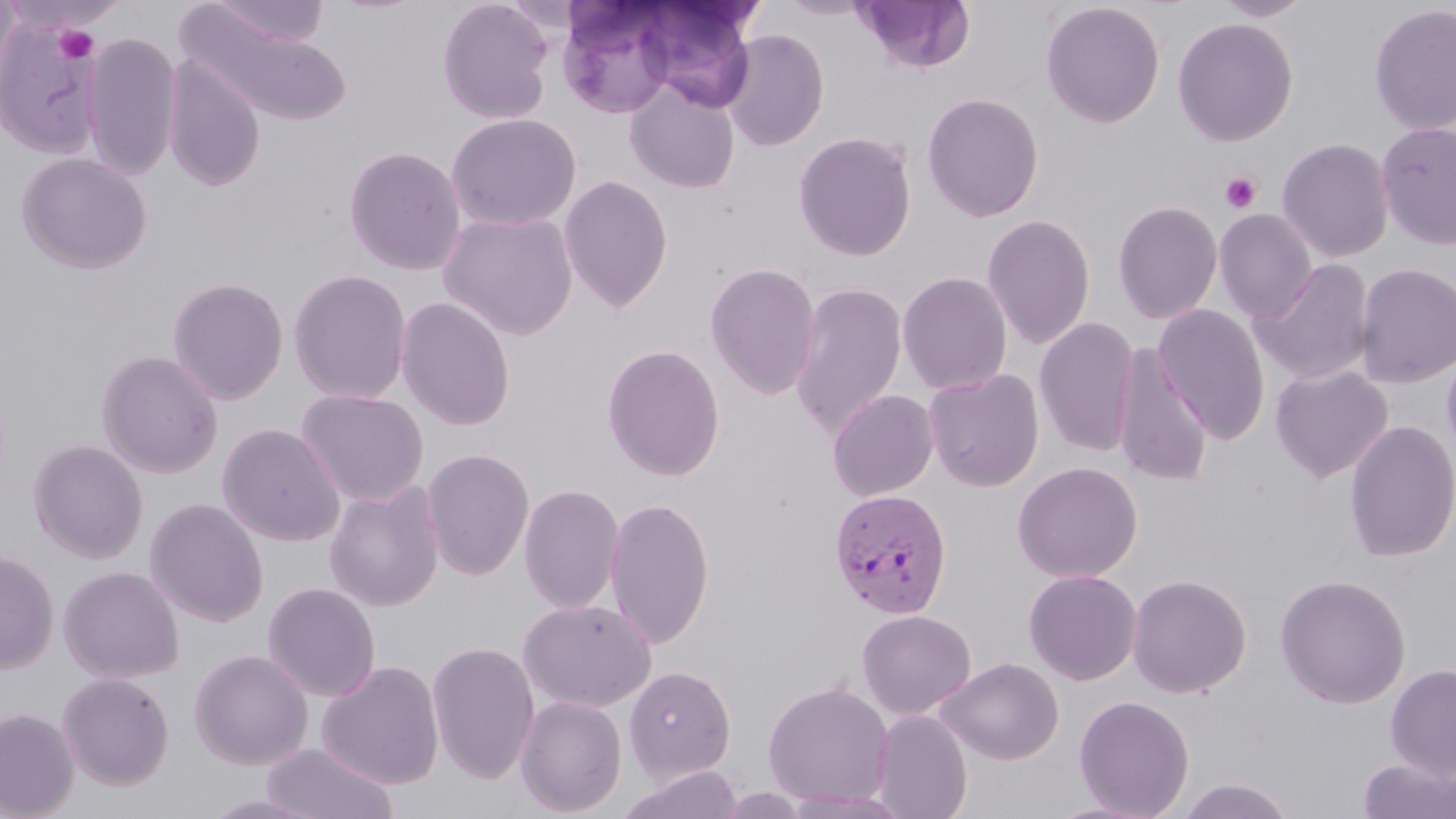

Summary:
  - Coordinate format: approximate bounding boxes as [x1, y1, x2, y2] in pixels
  - Platelet locations: [54, 24, 97, 62], [1220, 171, 1262, 214]
  - Plasmodium vivax-infected red blood cell locations: [828, 488, 953, 618]
  - Uninfected red blood cell locations: [0, 0, 23, 104], [208, 0, 331, 47], [437, 0, 555, 124], [776, 0, 877, 19], [854, 0, 977, 74], [1212, 0, 1317, 22], [633, 1, 759, 110], [1041, 1, 1165, 128], [558, 2, 678, 117], [1368, 3, 1456, 136], [179, 6, 351, 126], [0, 11, 105, 161], [1173, 17, 1298, 147], [720, 29, 829, 151], [83, 32, 182, 181], [162, 56, 266, 192], [625, 79, 741, 194], [922, 92, 1044, 223], [446, 113, 581, 231], [1376, 121, 1456, 251], [793, 131, 917, 262], [1277, 138, 1394, 263], [344, 145, 467, 276], [16, 152, 153, 275], [558, 174, 674, 313], [1112, 200, 1223, 325], [1214, 209, 1317, 322], [439, 210, 579, 340], [981, 213, 1096, 349], [1251, 259, 1376, 385], [704, 262, 822, 401], [1354, 262, 1456, 389], [289, 269, 412, 404], [897, 271, 1013, 395], [167, 277, 289, 404], [789, 281, 908, 440], [395, 297, 516, 431], [1153, 305, 1271, 444], [1034, 318, 1140, 457], [602, 343, 726, 482], [1441, 343, 1456, 464], [1112, 345, 1214, 488], [95, 349, 224, 478], [1270, 364, 1393, 483], [923, 369, 1045, 492], [296, 388, 430, 507], [826, 389, 940, 502], [1343, 420, 1456, 562], [217, 423, 346, 547], [27, 439, 148, 564], [421, 448, 535, 581], [1011, 462, 1142, 583], [324, 482, 445, 612], [518, 484, 625, 615], [604, 497, 715, 650], [144, 498, 269, 627], [0, 551, 59, 673], [58, 565, 184, 683], [1023, 569, 1142, 686], [1127, 572, 1252, 698], [1274, 573, 1412, 709], [262, 583, 381, 701], [517, 599, 656, 713], [856, 609, 976, 719], [426, 640, 540, 785], [189, 649, 313, 770], [937, 657, 1064, 765], [317, 660, 445, 790], [1385, 663, 1456, 779], [624, 666, 736, 783], [57, 672, 175, 790], [763, 681, 894, 809], [515, 695, 627, 816], [1073, 695, 1195, 818], [0, 708, 79, 819], [871, 710, 973, 819], [260, 743, 399, 819], [1357, 758, 1456, 819], [617, 764, 744, 819], [1175, 777, 1297, 819], [782, 789, 916, 817], [200, 791, 328, 818]
  - Slide-level diagnosis: Plasmodium vivax
  - Modality: optical microscopy
  - Field of view: one of a larger specimen
  - Stain: May-Grünwald-Giemsa
  - Image size: 1456×819 pixels
  - Magnification: 1000x
  - Preparation: thin blood smear